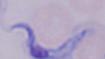
Summary:
  - Magnification: 1000x
  - Modality: photomicrograph
  - Identification: trypanosome